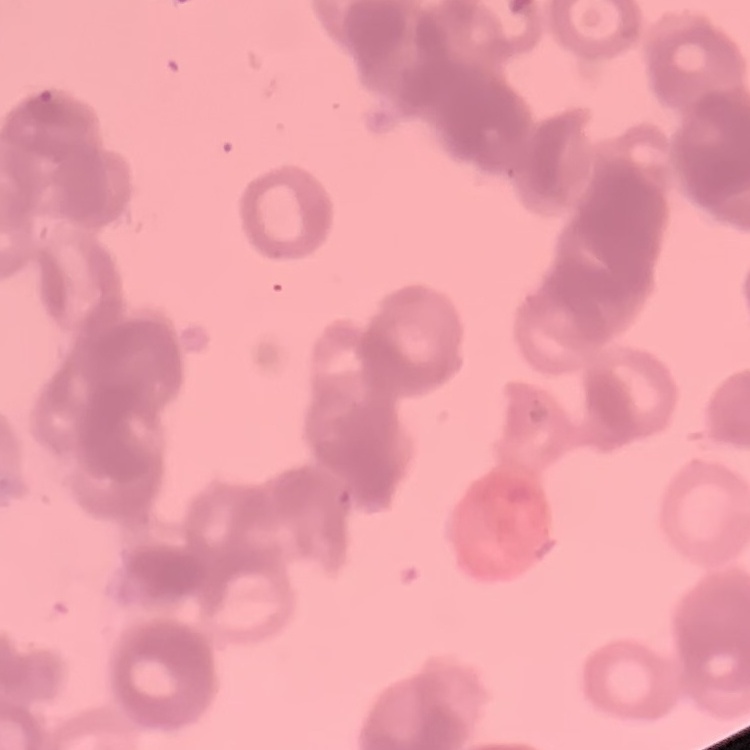

The red blood cells show rouleaux formation. Field's or Giemsa stain. Square crop of a larger photomicrograph. Thin peripheral smear.